Locate every Babesia divergens-infected red blood cell.
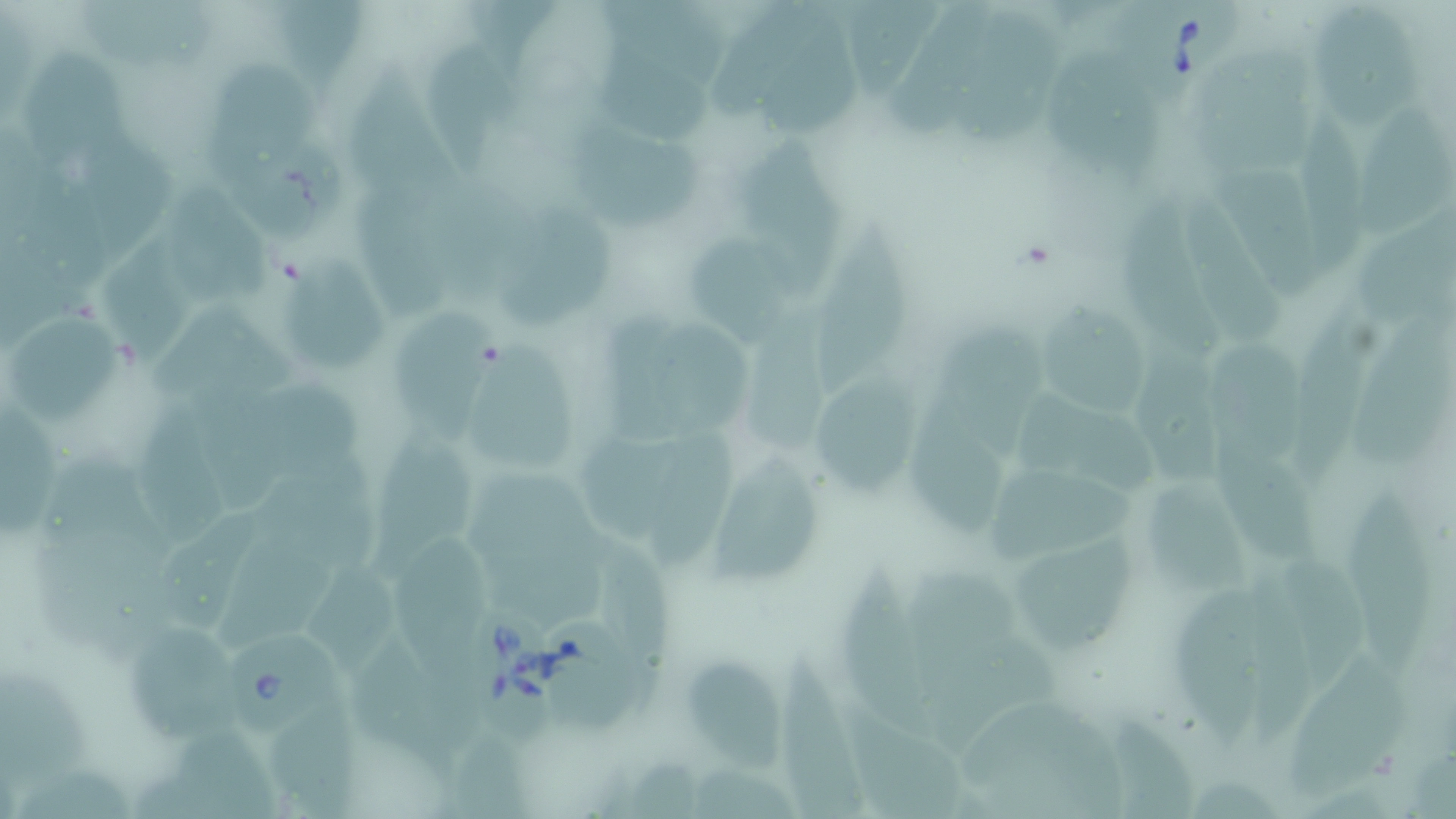

Approximate bounding boxes as (x1,y1)-(x2,y2) corner pairs in pixels.
Babesia divergens-infected red blood cells: (1117,0)-(1237,96), (464,590)-(558,749), (232,633)-(334,729).

slide-level diagnosis = Babesia divergens
modality = optical microscopy
preparation = thin blood smear
uninfected red blood cell locations = approximate bounding boxes as (x1,y1)-(x2,y2) corner pairs in pixels: (72,0)-(221,78), (276,0)-(366,89), (472,0)-(567,80), (601,0)-(724,61), (845,0)-(950,103), (890,0)-(1005,145), (1315,0)-(1418,128), (709,3)-(835,117), (949,5)-(1059,151), (764,18)-(867,145), (417,31)-(512,179), (605,41)-(719,141), (1196,45)-(1318,175), (28,47)-(141,167), (1044,49)-(1170,183), (212,55)-(322,167), (339,62)-(479,223), (1349,110)-(1453,245), (578,120)-(711,235), (84,127)-(178,254), (740,136)-(843,306), (228,137)-(340,241), (1224,152)-(1323,306), (17,163)-(114,302), (357,185)-(456,321), (1185,187)-(1282,347), (170,190)-(275,310), (1110,190)-(1231,371), (511,208)-(619,329), (1366,208)-(1456,332), (100,226)-(196,372), (819,227)-(916,403), (684,234)-(800,349), (291,259)-(389,369), (1042,299)-(1154,423), (390,301)-(503,442), (1295,301)-(1390,472), (741,302)-(833,459), (594,304)-(698,450), (154,306)-(298,406), (9,308)-(127,427), (1356,309)-(1456,461), (661,318)-(765,443), (942,318)-(1056,463), (1208,337)-(1310,473), (1127,338)-(1237,491), (471,344)-(579,470), (818,376)-(920,502), (249,380)-(359,483), (1001,383)-(1158,503), (904,388)-(1023,542), (189,392)-(294,510), (0,401)-(66,545), (141,404)-(232,549), (582,420)-(681,545), (647,425)-(741,568), (1223,427)-(1328,560), (371,432)-(472,582), (716,447)-(830,596), (271,451)-(394,581), (462,458)-(605,569), (984,460)-(1141,566), (1152,475)-(1262,601), (1344,482)-(1439,676), (158,502)-(267,635), (598,530)-(682,713), (1011,530)-(1138,655), (393,534)-(492,675), (220,537)-(334,660), (1273,541)-(1374,681), (311,554)-(413,682), (902,558)-(1022,704), (841,564)-(942,739), (1168,577)-(1276,743), (1249,577)-(1331,736), (916,619)-(1064,741), (550,621)-(646,741), (134,625)-(252,743), (343,631)-(469,773), (779,648)-(873,819), (689,655)-(787,786), (1289,659)-(1408,797), (0,661)-(95,794), (964,691)-(1126,800), (843,704)-(975,816), (275,707)-(371,819), (1109,712)-(1196,819), (176,725)-(283,817), (448,741)-(532,819), (700,750)-(798,819), (623,753)-(717,814)
image size = 1456×819 pixels
stain = May-Grünwald-Giemsa
magnification = 1000x
field of view = one of a larger specimen